Locate platelets.
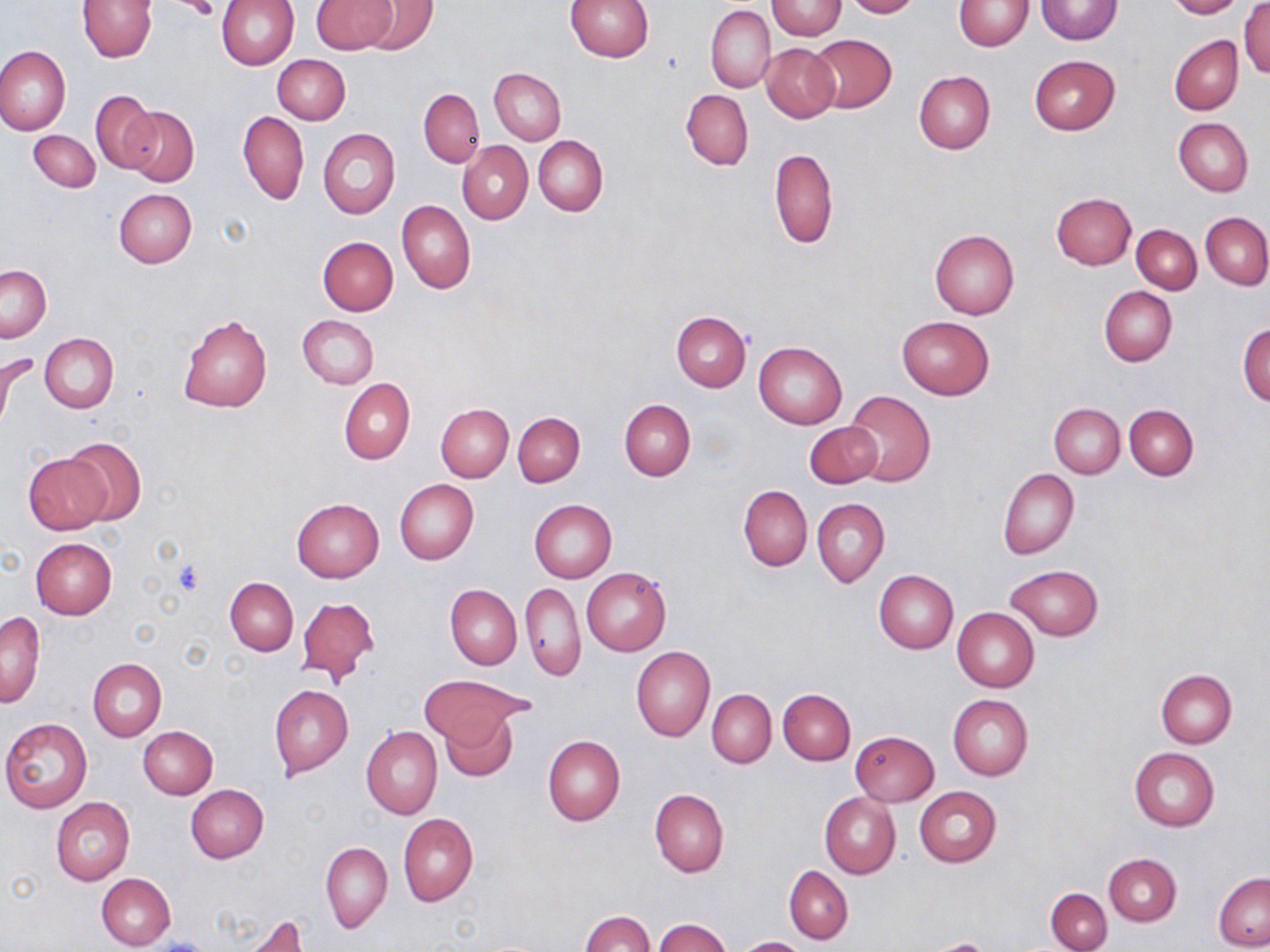

Approximate bounding boxes as (x1,y1)-(x2,y2) corner pairs in pixels.
Platelets: (177,1)-(218,21), (172,561)-(205,595).

Uninfected red blood cell locations: (215,0)-(299,70), (311,0)-(396,53), (364,0)-(437,55), (566,0)-(652,62), (842,0)-(920,18), (1037,0)-(1122,44), (1166,0)-(1246,18), (76,1)-(156,62), (768,1)-(845,40), (955,1)-(1032,51), (1239,3)-(1270,77), (705,5)-(775,94), (808,35)-(897,113), (1169,35)-(1243,115), (761,43)-(839,123), (0,46)-(71,135), (273,54)-(351,124), (1029,55)-(1120,135), (489,68)-(567,144), (914,71)-(995,154), (417,88)-(485,166), (90,90)-(158,173), (681,90)-(753,170), (122,106)-(198,186), (238,111)-(309,205), (1173,117)-(1253,195), (319,128)-(400,219), (29,129)-(101,192), (534,135)-(607,216), (458,141)-(533,223), (767,148)-(838,249), (114,188)-(196,268), (1051,193)-(1136,270), (398,201)-(476,294), (1201,213)-(1270,288), (1132,225)-(1201,294), (929,228)-(1019,320), (318,236)-(398,315), (1,265)-(51,342), (1099,285)-(1177,366), (671,311)-(750,391), (177,313)-(272,413), (298,315)-(378,389), (896,315)-(995,400), (1238,321)-(1269,407), (39,333)-(118,413), (754,341)-(847,429), (0,352)-(15,438), (339,378)-(415,464), (844,391)-(935,487), (619,399)-(695,480), (435,403)-(513,482), (1049,403)-(1124,478), (1125,404)-(1199,480), (513,411)-(584,487), (804,421)-(883,489), (63,436)-(147,526), (24,454)-(108,534), (998,468)-(1079,560), (394,479)-(479,565), (739,485)-(812,571), (291,497)-(384,582), (813,498)-(889,587), (529,499)-(616,583), (30,537)-(117,618), (1005,564)-(1103,640), (581,566)-(671,656), (874,569)-(958,653), (225,577)-(298,655), (521,582)-(584,680), (446,584)-(521,669), (297,596)-(379,684), (953,607)-(1039,692), (1,611)-(45,707), (631,646)-(715,741), (87,658)-(167,741), (1155,668)-(1237,748), (420,676)-(524,743), (269,684)-(353,777), (778,688)-(856,764), (706,689)-(776,768), (947,693)-(1033,781), (437,709)-(517,782), (1,717)-(92,812), (139,725)-(218,798), (361,726)-(442,819), (850,730)-(939,806), (544,735)-(625,824), (1129,747)-(1220,831), (186,783)-(268,862), (914,786)-(1001,867), (650,787)-(729,877), (819,793)-(901,879), (52,799)-(134,884), (398,813)-(478,907), (321,842)-(392,933), (1104,854)-(1181,925), (784,865)-(853,945), (97,872)-(176,950), (1213,872)-(1270,950), (1045,887)-(1112,952), (579,910)-(654,952), (238,914)-(310,952), (655,918)-(732,952), (736,937)-(805,952). Slide-level diagnosis: negative for blood parasites. May-Grünwald-Giemsa-stained preparation. Single field of view. Image is 1270×952 pixels. Thin blood film. Optical microscopy. Captured at 1000x magnification.